State which parasite is depicted.
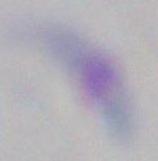

Toxoplasma gondii.

Summary:
  - Modality: micrograph
  - Magnification: 1000x